Report the malaria status of this cell.
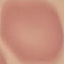
It is uninfected.

Giemsa-stained preparation. Thin smear of blood. Cell patch, automatically extracted from a larger field of view and resized to 64 × 64 pixels. Acquired by smartphone through the microscope eyepiece.